Assess this cell for malaria.
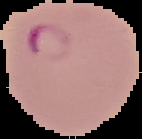
Parasitized.

Summary:
  - Image size: 142×139 pixels
  - Image type: segmented cell region with the area outside set to black
  - Preparation: thin blood film